Describe the morphology of the erythrocytes.
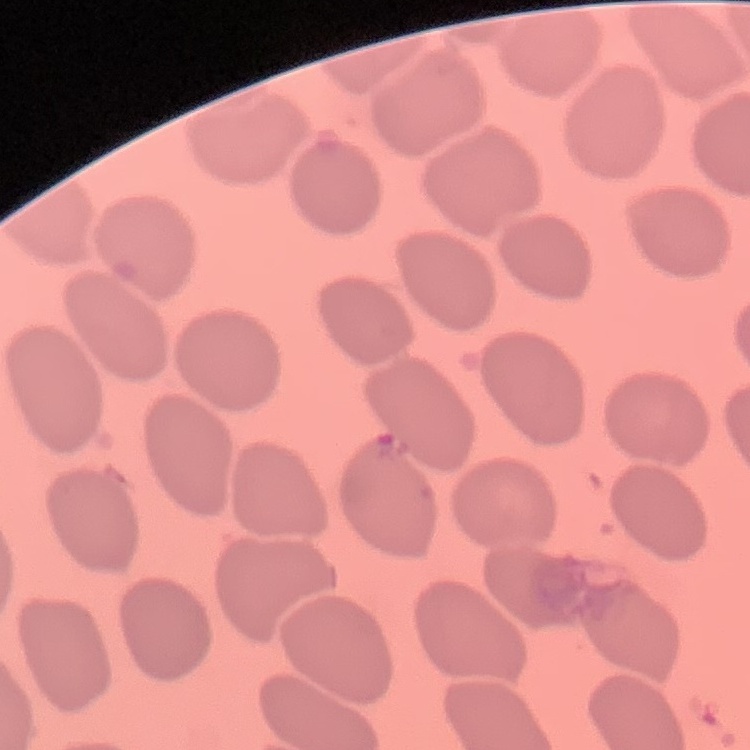

They show no rouleaux formation.

image_type: square crop of a larger photomicrograph
stain: Field's or Giemsa
preparation: thin peripheral smear